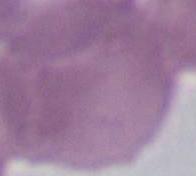
Summary:
  - Magnification: 1000x
  - Identification: erythrocyte
  - Modality: micrograph